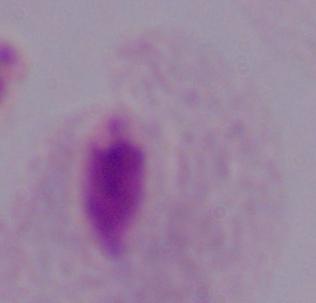
modality = photomicrograph
magnification = 1000x
identification = trichomonad